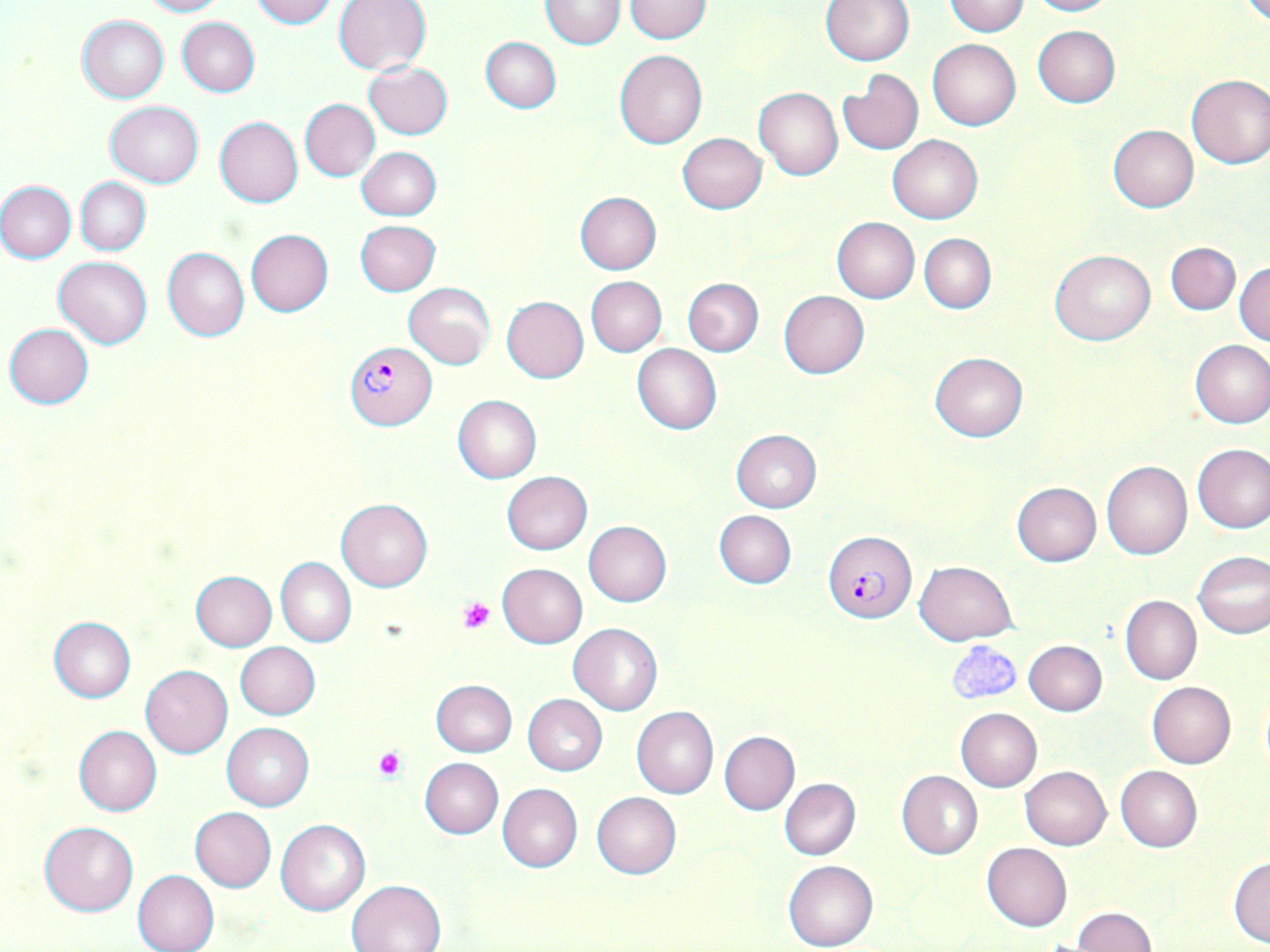
Plasmodium falciparum-infected red blood cell locations = approximate bounding boxes as (x1, y1, x2, y2) in pixels: (344, 343, 436, 429), (824, 531, 916, 623)
slide-level diagnosis = Plasmodium falciparum
magnification = 1000x
stain = May-Grünwald-Giemsa
modality = optical microscopy
preparation = thin blood film
field of view = single
platelet locations = approximate bounding boxes as (x1, y1, x2, y2) in pixels: (459, 598, 495, 633), (947, 640, 1022, 704), (373, 746, 408, 781)
image size = 1270×952 pixels
uninfected red blood cell locations = approximate bounding boxes as (x1, y1, x2, y2) in pixels: (137, 0, 226, 17), (250, 0, 337, 27), (333, 0, 431, 75), (820, 0, 915, 65), (942, 0, 1029, 35), (1024, 0, 1117, 16), (541, 1, 625, 49), (624, 1, 713, 43), (76, 15, 169, 103), (177, 17, 260, 97), (1032, 25, 1121, 108), (480, 37, 561, 113), (927, 39, 1020, 130), (614, 50, 708, 149), (363, 61, 453, 139), (836, 70, 924, 154), (1185, 74, 1270, 168), (754, 86, 843, 180), (299, 99, 380, 181), (105, 101, 204, 187), (215, 116, 303, 208), (1108, 124, 1199, 212), (677, 133, 766, 214), (886, 135, 983, 224), (356, 147, 442, 221), (76, 177, 151, 255), (0, 180, 76, 263), (574, 192, 661, 274), (831, 216, 920, 302), (355, 219, 440, 295), (246, 229, 334, 316), (919, 233, 996, 313), (1165, 242, 1240, 314), (162, 247, 250, 341), (1049, 248, 1155, 345), (54, 256, 152, 348), (1234, 261, 1270, 346), (585, 276, 667, 355), (682, 277, 764, 357), (403, 282, 495, 367), (778, 291, 868, 378), (503, 296, 589, 382), (4, 323, 93, 408), (1190, 340, 1270, 429), (632, 343, 723, 434), (929, 352, 1029, 442), (452, 395, 541, 483), (730, 429, 822, 512), (1192, 443, 1270, 533), (1101, 461, 1192, 560), (501, 470, 592, 554), (1011, 482, 1101, 567), (336, 498, 433, 591), (713, 509, 797, 588), (583, 520, 672, 606), (1193, 550, 1270, 639), (275, 557, 355, 647), (915, 560, 1017, 644), (497, 563, 587, 648), (191, 571, 277, 650), (1120, 594, 1201, 685), (48, 618, 136, 702), (568, 622, 662, 715), (1024, 640, 1108, 716), (235, 642, 319, 720), (141, 665, 233, 758), (430, 680, 516, 756), (1147, 682, 1236, 769), (523, 694, 607, 775), (632, 706, 718, 798), (955, 708, 1042, 792), (221, 722, 315, 811), (73, 725, 162, 816), (718, 731, 800, 815), (420, 758, 503, 838), (1115, 765, 1203, 852), (1020, 766, 1111, 850), (897, 770, 983, 859), (779, 778, 861, 860), (498, 783, 582, 873), (592, 792, 681, 879), (190, 807, 276, 892), (276, 819, 370, 915), (40, 821, 139, 916), (982, 843, 1072, 931), (1228, 856, 1270, 947), (783, 859, 877, 951), (133, 869, 220, 952), (346, 879, 447, 952), (1072, 907, 1157, 951)